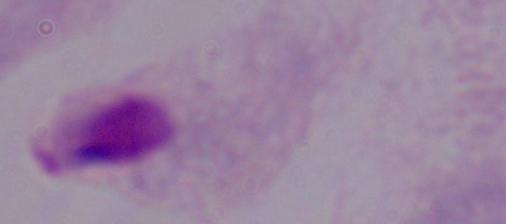

Summary:
  - Identification: trichomonad
  - Modality: photomicrograph
  - Magnification: 1000x